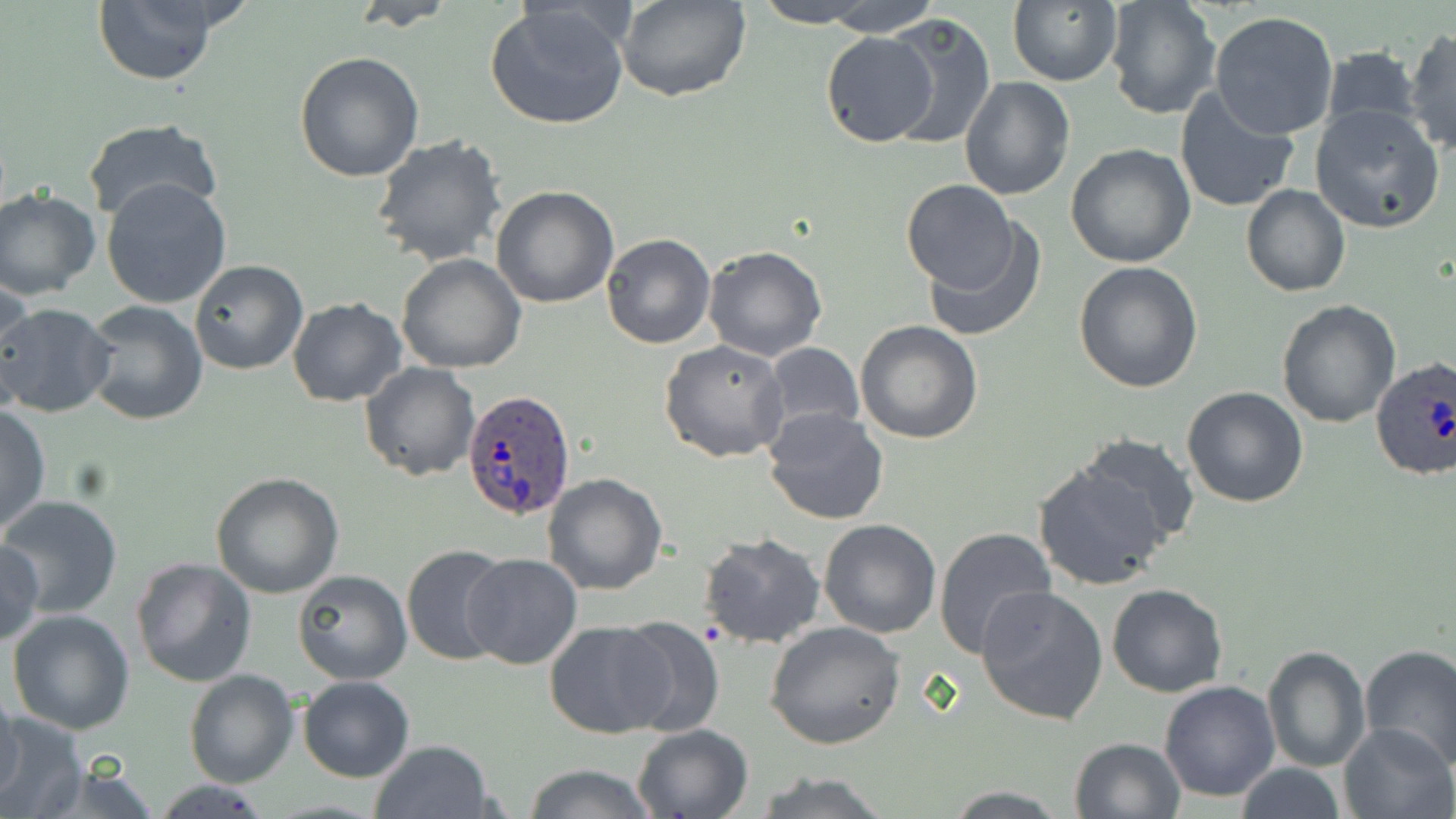
Summary:
  - Coordinate format: approximate bounding boxes as (x1,y1)-(x2,y2) corner pairs in pixels
  - Plasmodium ovale-infected red blood cell locations: (1371,357)-(1456,484), (463,391)-(576,520)
  - Uninfected red blood cell locations: (93,0)-(222,86), (824,0)-(941,36), (1008,0)-(1123,88), (1105,0)-(1221,121), (349,1)-(459,29), (483,1)-(631,132), (615,1)-(751,103), (750,1)-(876,27), (1209,11)-(1341,141), (881,14)-(997,150), (1405,29)-(1456,155), (820,31)-(939,147), (1351,38)-(1456,150), (1320,45)-(1420,135), (294,51)-(424,182), (959,76)-(1075,201), (1173,83)-(1302,215), (1308,104)-(1445,234), (82,118)-(225,228), (370,135)-(508,267), (1065,144)-(1197,268), (101,179)-(232,309), (901,180)-(1017,294), (1241,184)-(1351,297), (0,186)-(100,301), (491,186)-(619,308), (919,218)-(1047,343), (602,233)-(716,349), (702,245)-(829,362), (395,253)-(526,373), (190,259)-(309,374), (1073,262)-(1204,394), (666,265)-(804,434), (0,283)-(35,404), (287,296)-(407,406), (1275,298)-(1401,428), (79,300)-(208,426), (0,303)-(117,417), (854,321)-(984,444), (658,339)-(789,463), (763,343)-(866,441), (359,362)-(480,481), (1182,386)-(1309,509), (0,406)-(49,535), (762,408)-(889,526), (1073,431)-(1201,549), (1031,462)-(1173,591), (211,471)-(344,597), (543,472)-(670,595), (2,495)-(123,618), (820,520)-(941,638), (933,527)-(1057,661), (698,533)-(827,649), (1,540)-(46,647), (400,541)-(512,667), (462,554)-(584,670), (130,557)-(256,687), (292,569)-(412,685), (1106,584)-(1228,698), (976,585)-(1109,724), (6,608)-(136,735), (611,614)-(725,737), (544,619)-(673,740), (764,620)-(907,750), (1359,644)-(1456,768), (1263,646)-(1370,772), (183,669)-(300,788), (297,676)-(414,783), (1159,680)-(1280,803), (0,689)-(23,802), (0,711)-(89,817), (1336,721)-(1456,819), (631,723)-(754,818), (1068,736)-(1186,819), (369,739)-(495,819), (23,758)-(164,819), (522,763)-(660,818), (1232,763)-(1347,819), (749,770)-(894,819), (152,778)-(272,818), (940,786)-(1075,817)
  - Slide-level diagnosis: Plasmodium ovale
  - Magnification: 1000x
  - Image size: 1456×819 pixels
  - Stain: May-Grünwald-Giemsa
  - Preparation: thin blood film
  - Modality: optical microscopy
  - Field of view: one of a larger specimen